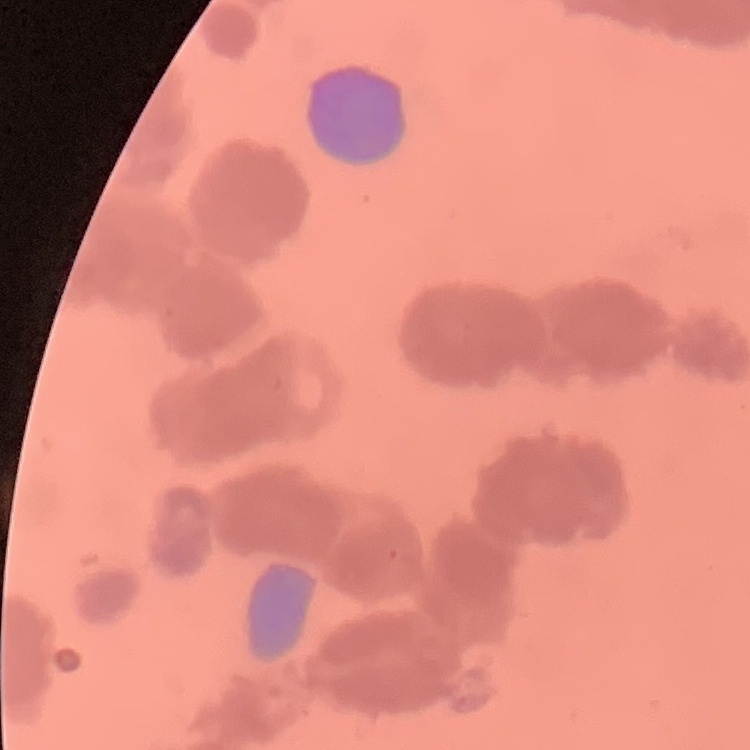
erythrocyte_morphology: rouleaux formation
image_type: one tile cut from a larger photomicrograph
stain: Field's or Giemsa
preparation: thin blood film